Give the extent of all Plasmodium falciparum-infected red blood cells.
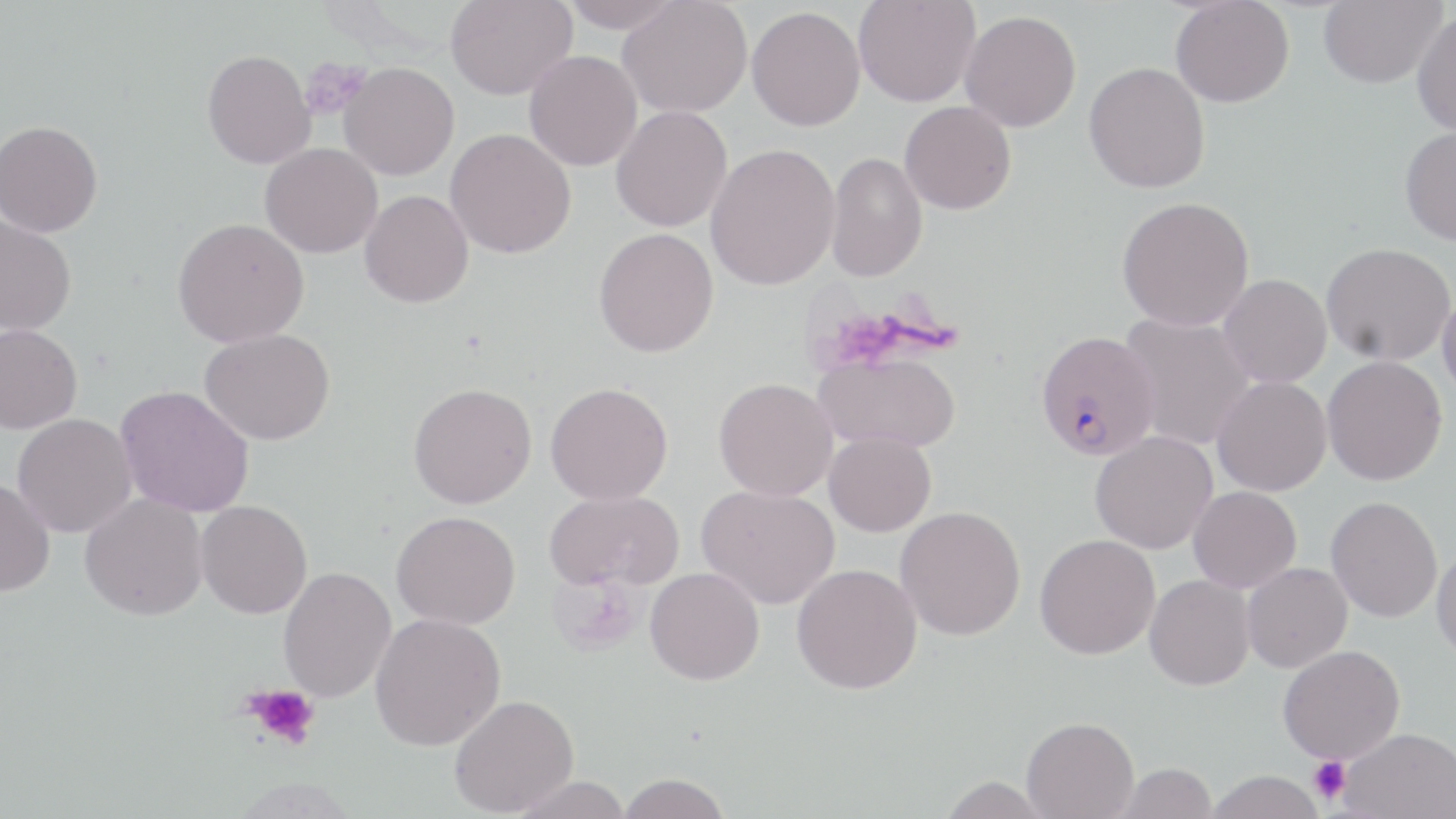

Approximate bounding boxes as (x1, y1, x2, y2) in pixels.
Plasmodium falciparum-infected red blood cells: (1035, 330, 1160, 460).

Summary:
  - Uninfected red blood cell locations: (444, 0, 578, 101), (559, 0, 682, 33), (618, 0, 752, 118), (853, 0, 980, 108), (1170, 0, 1294, 108), (1319, 0, 1446, 88), (747, 6, 865, 131), (959, 10, 1081, 132), (1411, 11, 1456, 137), (201, 50, 315, 170), (524, 50, 642, 171), (338, 62, 459, 180), (1083, 62, 1210, 193), (899, 101, 1017, 215), (610, 105, 732, 232), (0, 119, 103, 237), (1399, 126, 1456, 246), (444, 128, 576, 259), (259, 143, 383, 258), (705, 143, 840, 291), (825, 151, 928, 282), (360, 190, 474, 308), (1116, 196, 1255, 332), (0, 215, 77, 336), (172, 217, 309, 348), (593, 228, 718, 357), (1320, 242, 1455, 367), (1217, 274, 1332, 388), (1437, 289, 1456, 401), (1118, 312, 1256, 450), (0, 324, 82, 434), (199, 329, 335, 445), (814, 350, 961, 453), (1321, 356, 1447, 486), (1212, 376, 1332, 496), (713, 378, 838, 501), (408, 382, 537, 509), (545, 382, 673, 505), (115, 385, 255, 517), (11, 413, 137, 538), (824, 431, 936, 537), (1090, 431, 1217, 554), (0, 479, 56, 597), (696, 484, 839, 609), (1187, 486, 1301, 593), (544, 489, 683, 592), (79, 494, 208, 621), (1325, 496, 1443, 622), (196, 500, 312, 619), (895, 505, 1026, 641), (391, 510, 520, 629), (1035, 534, 1160, 660), (1431, 544, 1456, 662), (1242, 562, 1352, 673), (791, 563, 922, 695), (277, 566, 397, 703), (645, 566, 764, 685), (1144, 574, 1255, 690), (369, 612, 506, 751), (1278, 645, 1405, 764), (449, 694, 579, 816), (1021, 716, 1139, 818), (1339, 727, 1455, 819), (1114, 762, 1217, 819), (1204, 769, 1326, 819), (616, 773, 731, 818), (508, 775, 635, 819), (935, 776, 1054, 818)
  - Platelet locations: (299, 57, 369, 120), (243, 682, 321, 750), (1308, 756, 1351, 805)
  - Slide-level diagnosis: Plasmodium falciparum
  - Image size: 1456×819 pixels
  - Modality: optical microscopy
  - Stain: May-Grünwald-Giemsa
  - Magnification: 1000x
  - Preparation: thin blood film
  - Field of view: one of a larger specimen